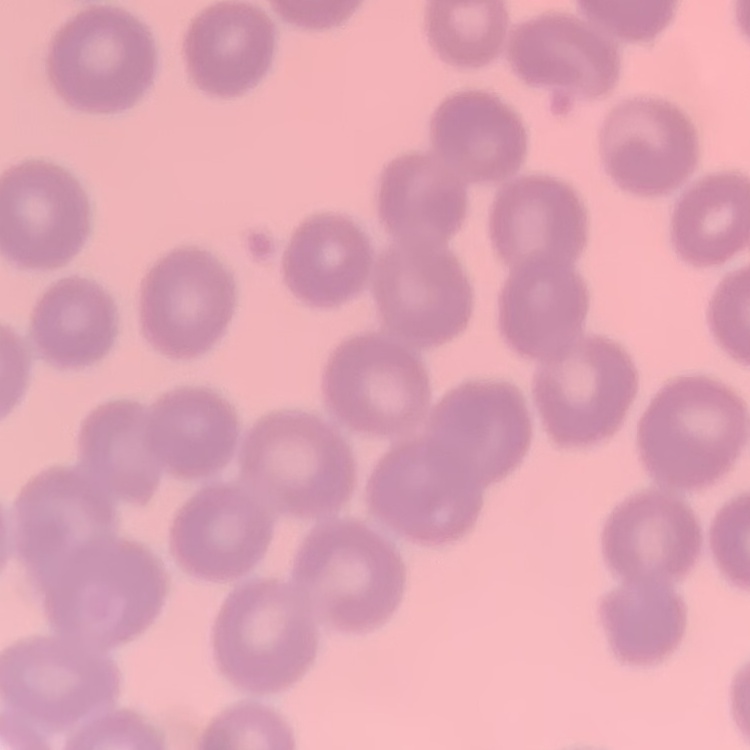
erythrocyte morphology = no rouleaux formation
image type = one tile cut from a larger photomicrograph
stain = Field's or Giemsa
preparation = thin peripheral smear